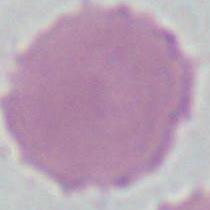
Photomicrograph. Captured at 1000x magnification. An erythrocyte is shown.